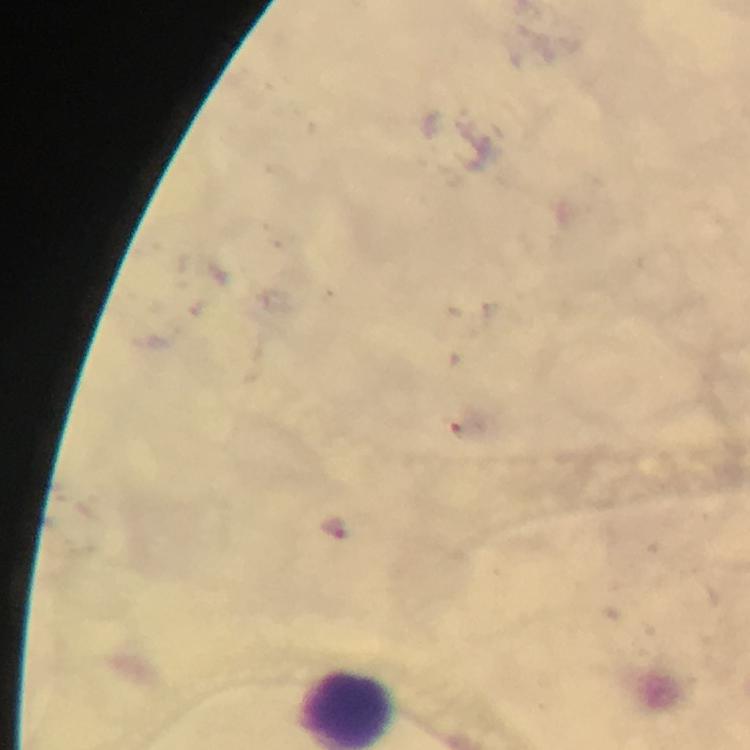
cropped_from: one field of view
preparation: thick blood film
malaria_parasite_locations: 'approximate centers as [x, y] in pixels: [333, 527]'
context: from a diagnostic examination for malaria
stain: Giemsa
immersion_oil: applied
image_size: 750×750 pixels
magnification: 100x
capture: smartphone camera through the microscope